Describe the morphology of the erythrocytes.
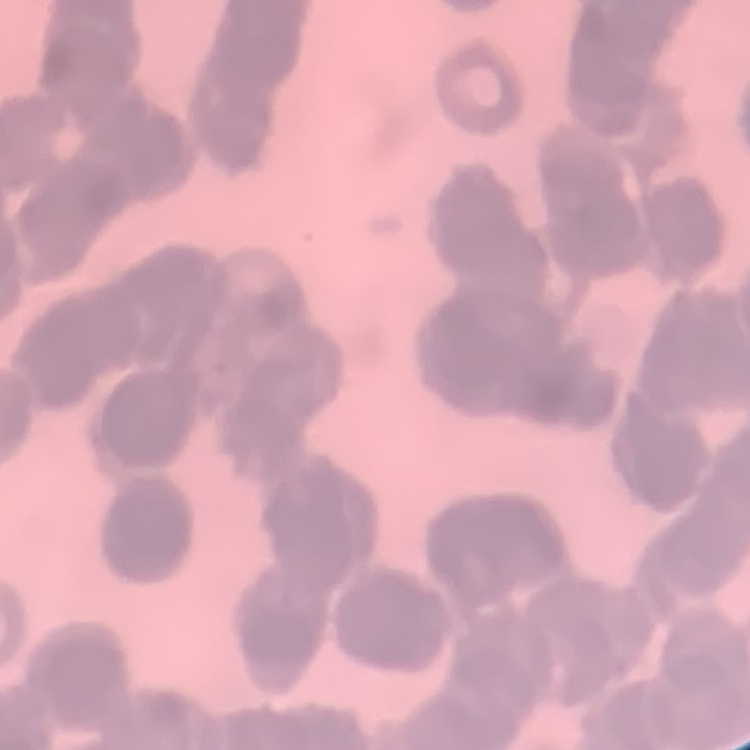

They show rouleaux formation.

stain = Field's or Giemsa
preparation = thin blood film
image type = one tile cut from a larger photomicrograph